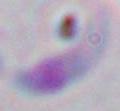
Micrograph. Toxoplasma gondii is seen. Captured at 1000x magnification.